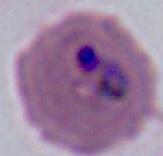

{
  "magnification": "400x or 1000x",
  "identification": "Plasmodium",
  "modality": "photomicrograph"
}